Name the blood parasite species.
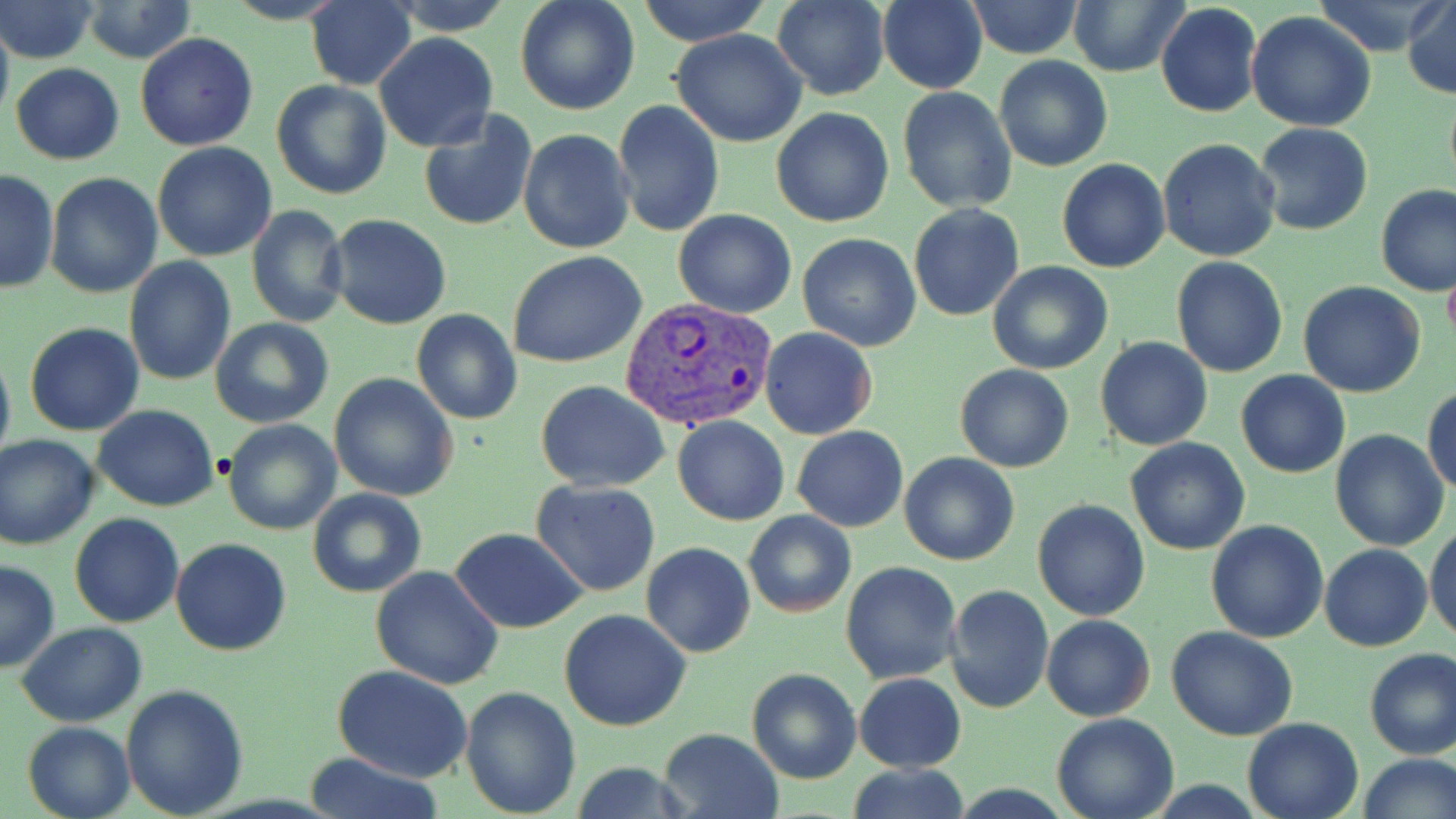
Plasmodium vivax.

Summary:
  - Coordinate format: approximate bounding boxes as [x1, y1, x2, y2] in pixels
  - Uninfected red blood cell locations: [2, 0, 100, 64], [304, 0, 417, 89], [390, 0, 513, 36], [514, 0, 640, 116], [636, 0, 771, 47], [773, 0, 887, 101], [878, 0, 986, 93], [1067, 0, 1190, 75], [1313, 0, 1437, 53], [966, 1, 1084, 59], [1403, 1, 1455, 98], [1155, 4, 1263, 118], [75, 5, 198, 62], [1246, 11, 1377, 131], [0, 12, 14, 128], [672, 29, 807, 147], [135, 31, 257, 151], [373, 33, 498, 153], [993, 55, 1113, 172], [10, 63, 125, 165], [271, 81, 391, 201], [897, 87, 1016, 213], [610, 101, 725, 237], [771, 108, 894, 228], [419, 110, 538, 232], [1254, 123, 1373, 237], [517, 128, 636, 255], [1156, 138, 1282, 262], [151, 143, 277, 262], [1058, 158, 1171, 273], [1, 169, 60, 296], [45, 172, 163, 298], [1374, 183, 1456, 297], [246, 204, 349, 329], [908, 204, 1024, 321], [674, 210, 797, 318], [326, 213, 451, 329], [798, 232, 923, 351], [508, 251, 647, 368], [1172, 256, 1289, 376], [123, 257, 236, 386], [987, 261, 1113, 374], [1443, 261, 1456, 350], [1298, 281, 1427, 399], [410, 309, 522, 424], [210, 317, 334, 427], [24, 322, 145, 437], [758, 328, 878, 440], [1096, 337, 1214, 452], [0, 346, 15, 471], [954, 364, 1074, 472], [1235, 369, 1351, 479], [329, 373, 459, 502], [537, 381, 669, 492], [1423, 384, 1456, 496], [92, 405, 219, 512], [673, 414, 789, 526], [222, 418, 341, 535], [791, 425, 908, 531], [1329, 430, 1449, 551], [0, 435, 100, 550], [1125, 438, 1251, 555], [900, 451, 1019, 567], [531, 481, 662, 599], [309, 488, 426, 598], [1031, 498, 1150, 621], [744, 510, 855, 618], [70, 512, 185, 628], [1204, 520, 1328, 643], [1427, 523, 1456, 643], [68, 524, 291, 637], [451, 528, 585, 633], [170, 538, 292, 657], [641, 542, 756, 657], [1320, 544, 1433, 651], [0, 560, 59, 672], [841, 561, 961, 685], [370, 563, 504, 691], [944, 584, 1055, 714], [558, 609, 692, 732], [1042, 615, 1156, 722], [16, 621, 148, 727], [1166, 626, 1298, 742], [1364, 648, 1456, 760], [333, 665, 474, 783], [748, 668, 861, 783], [854, 673, 966, 772], [120, 683, 249, 817], [460, 686, 581, 815], [1052, 712, 1179, 819], [1242, 716, 1365, 819], [22, 720, 134, 819], [658, 728, 783, 819], [304, 752, 445, 819], [1356, 752, 1455, 819], [568, 761, 696, 819], [846, 765, 972, 819]
  - Plasmodium vivax-infected red blood cell locations: [617, 297, 777, 431]
  - Modality: optical microscopy
  - Magnification: 1000x
  - Field of view: single
  - Image size: 1456×819 pixels
  - Stain: May-Grünwald-Giemsa
  - Preparation: thin blood smear